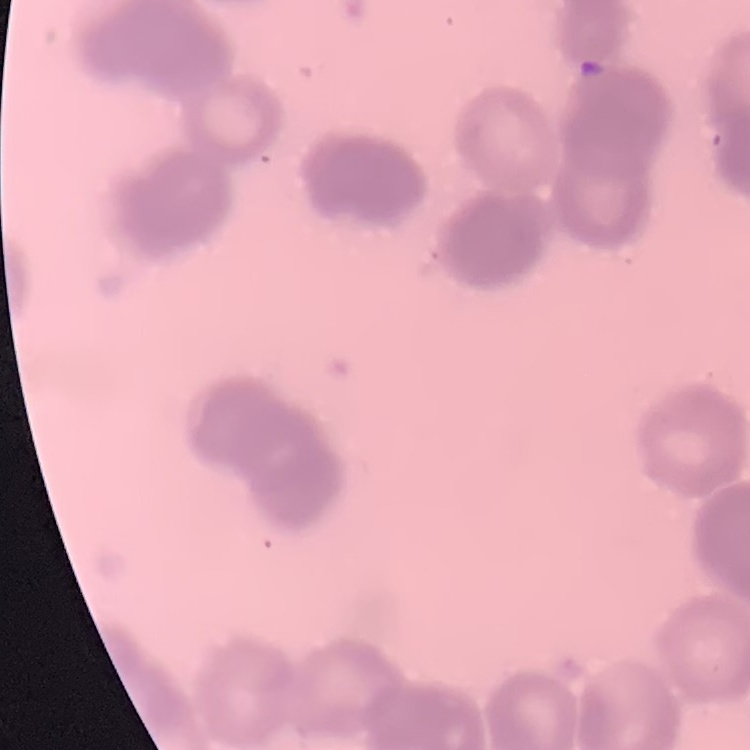

red blood cell morphology = rouleaux formation
preparation = thin blood film
stain = Field's or Giemsa
image type = one tile cut from a larger photomicrograph